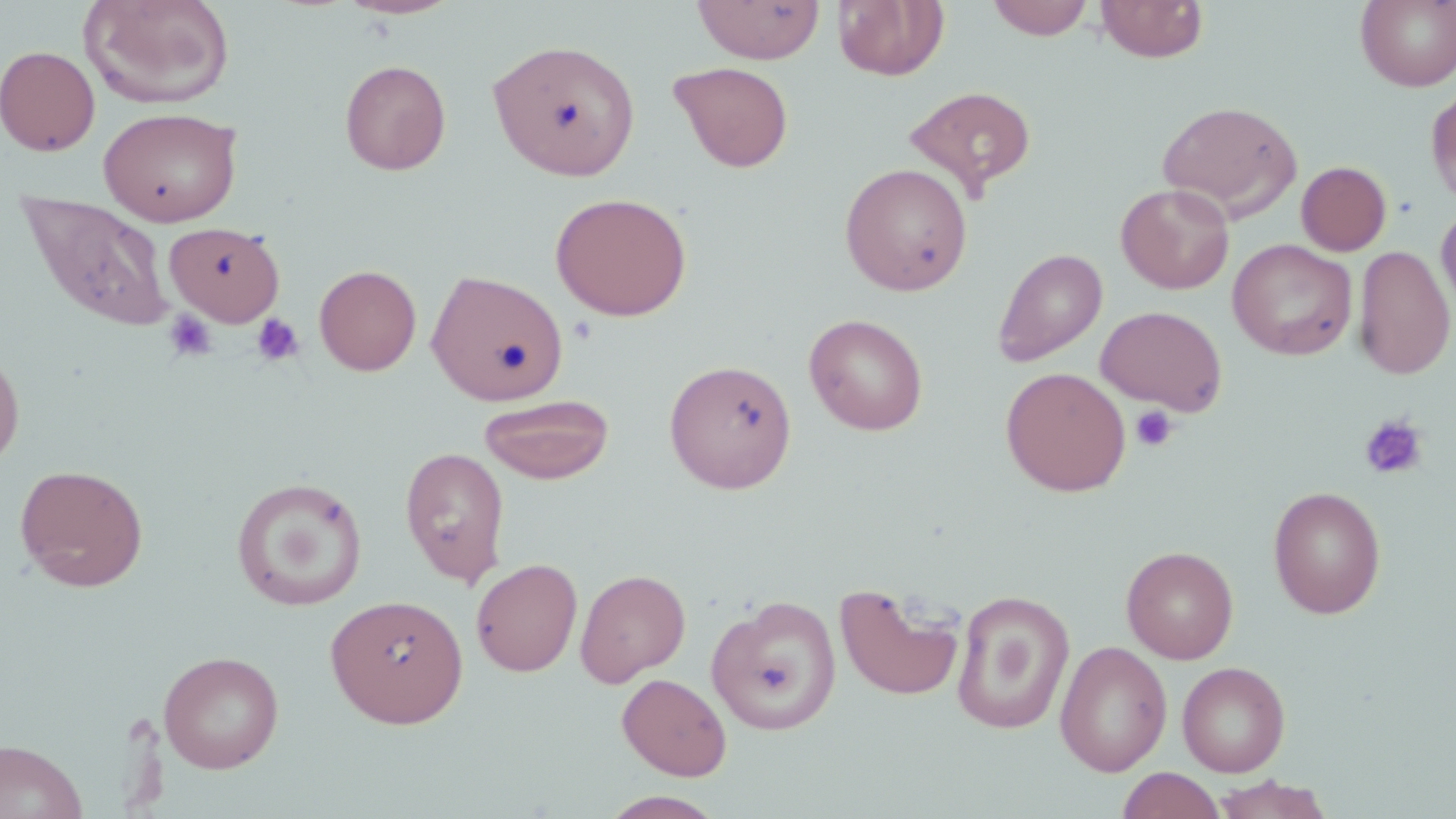
Approximate bounding boxes as (x1,y1)-(x2,y2) corner pairs in pixels. Platelet locations: (163,310)-(218,363), (251,313)-(305,367), (1130,405)-(1178,452), (1359,415)-(1428,479). Uninfected red blood cell locations: (79,0)-(236,109), (338,0)-(460,20), (987,0)-(1093,40), (1096,0)-(1208,63), (694,1)-(824,64), (834,1)-(950,81), (1355,1)-(1455,91), (487,39)-(640,181), (0,45)-(100,157), (340,59)-(452,175), (669,61)-(794,173), (904,85)-(1037,197), (1427,88)-(1456,207), (1156,99)-(1302,220), (98,107)-(242,226), (1296,160)-(1392,256), (839,163)-(973,296), (1116,183)-(1235,294), (17,190)-(176,335), (551,192)-(693,321), (1436,203)-(1456,316), (163,221)-(286,326), (1228,239)-(1357,360), (1354,245)-(1455,380), (992,248)-(1107,367), (314,264)-(422,375), (427,269)-(568,406), (1096,305)-(1227,415), (804,313)-(928,435), (0,343)-(25,472), (664,358)-(797,494), (1001,367)-(1131,496), (478,394)-(615,484), (400,445)-(510,587), (14,463)-(149,592), (231,477)-(368,611), (1267,485)-(1386,619), (1121,545)-(1239,664), (471,558)-(582,677), (575,568)-(691,686), (834,581)-(965,702), (952,590)-(1075,735), (325,593)-(469,728), (706,594)-(842,736), (1054,640)-(1173,776), (158,650)-(284,774), (1177,661)-(1290,777), (617,673)-(732,780), (0,739)-(87,819), (1117,768)-(1226,819), (1210,776)-(1334,819), (598,790)-(728,818). Slide-level diagnosis: negative for blood parasites. Image is 1456×819 pixels. Thin blood film. 1000x magnification. Optical microscopy. May-Grünwald-Giemsa stain. One field of a larger specimen.